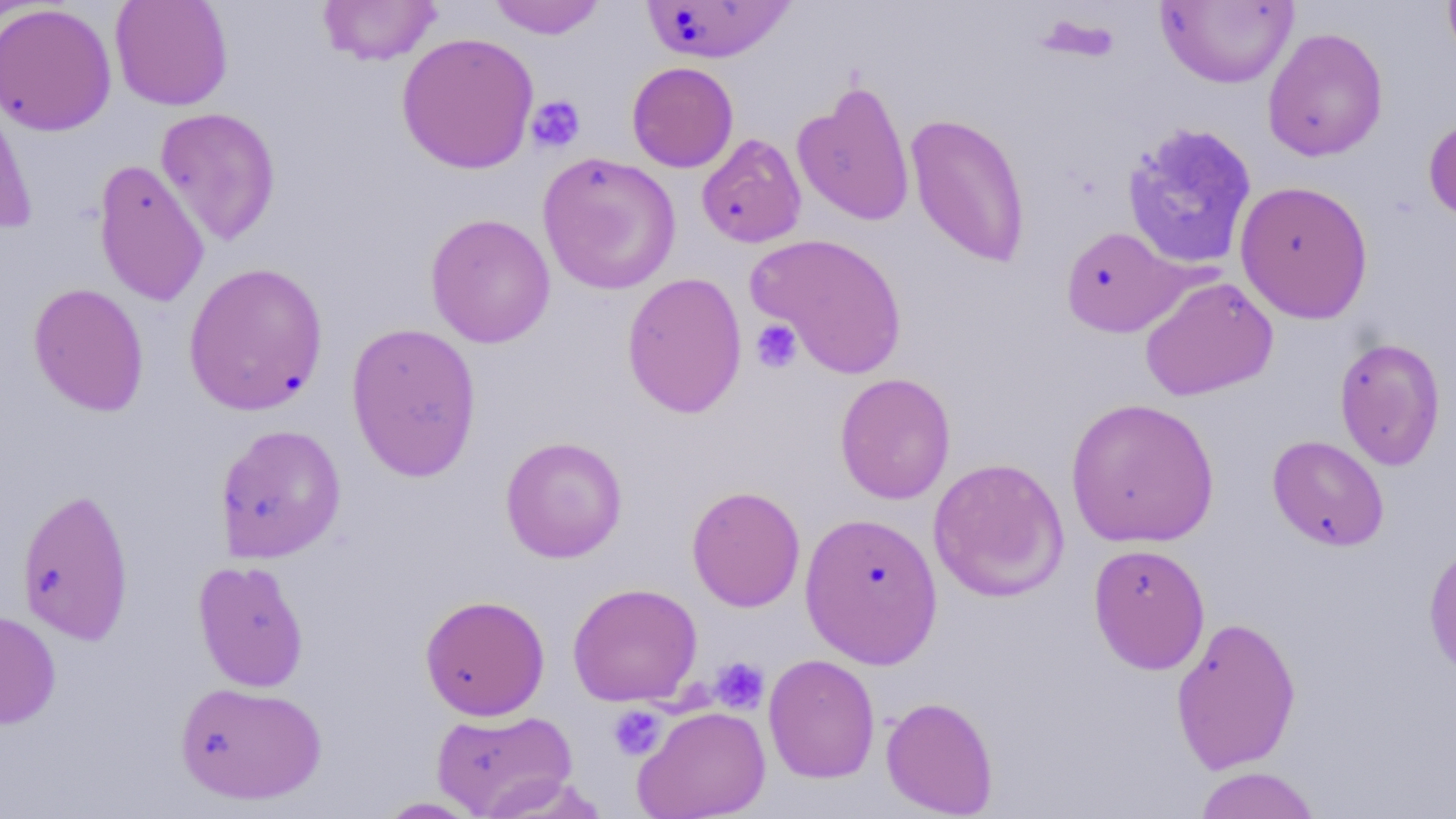

Summary:
  - Coordinate format: approximate bounding boxes as (x1,y1)-(x2,y2) corner pairs in pixels
  - Uninfected red blood cell locations: (110,0)-(233,111), (317,0)-(441,66), (487,0)-(606,39), (1442,0)-(1456,68), (641,1)-(795,63), (1156,1)-(1298,89), (0,3)-(117,136), (1261,27)-(1389,162), (396,32)-(540,175), (626,61)-(739,172), (0,75)-(37,234), (791,79)-(916,228), (155,107)-(281,247), (1423,112)-(1456,226), (904,113)-(1032,268), (1121,121)-(1258,271), (696,133)-(807,248), (537,153)-(681,295), (93,159)-(209,307), (1234,179)-(1374,324), (425,213)-(556,348), (1060,225)-(1191,338), (746,232)-(908,379), (183,261)-(328,416), (622,271)-(748,418), (1139,276)-(1278,400), (27,282)-(149,417), (345,321)-(483,482), (1334,336)-(1447,471), (834,372)-(956,505), (1065,397)-(1220,548), (215,423)-(347,563), (500,435)-(628,563), (1267,435)-(1390,551), (928,456)-(1069,602), (686,485)-(806,612), (16,487)-(135,645), (799,511)-(944,668), (1422,537)-(1456,685), (1088,542)-(1211,674), (192,559)-(310,692), (566,582)-(703,707), (419,593)-(550,721), (0,610)-(61,730), (1170,615)-(1302,775), (763,653)-(880,783), (174,680)-(327,805), (880,695)-(999,817), (633,705)-(771,819), (431,708)-(578,818), (1193,766)-(1322,818), (374,797)-(487,818)
  - Platelet locations: (526,95)-(585,153), (751,318)-(802,373), (710,657)-(769,713), (607,705)-(667,761)
  - Slide-level diagnosis: no evidence of blood parasites
  - Image size: 1456×819 pixels
  - Field of view: single
  - Stain: May-Grünwald-Giemsa
  - Magnification: 1000x
  - Preparation: thin blood smear
  - Modality: optical microscopy